Find each white blood cell.
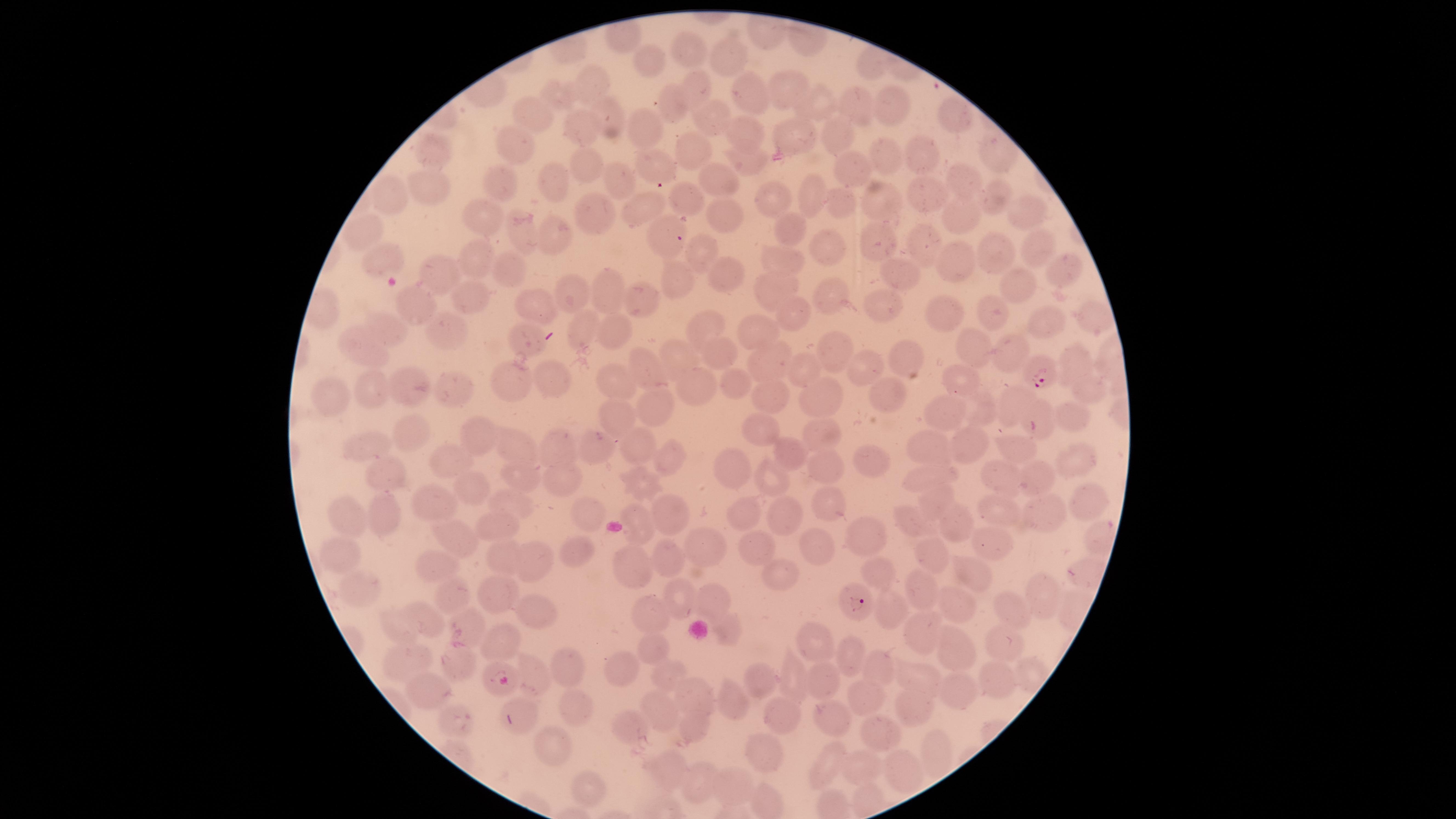

No white blood cells identified.

Approximate marker points as (x, y) in pixels. Parasitized red blood cells: (654, 169), (670, 237), (1041, 369), (854, 596). Uninfected red blood cells: (692, 49), (728, 56), (649, 60), (599, 82), (697, 87), (789, 87), (748, 93), (561, 94), (820, 102), (888, 102), (672, 105), (857, 105), (530, 113), (609, 118), (958, 118), (711, 120), (643, 123), (748, 130), (582, 131), (793, 133), (839, 133), (514, 140), (434, 149), (693, 151), (993, 154), (888, 155), (750, 157), (923, 158), (845, 163), (587, 166), (554, 177), (618, 177), (710, 178), (963, 178), (500, 183), (427, 185), (921, 193), (388, 194), (995, 194), (811, 196), (878, 196), (687, 199), (844, 201), (772, 202), (638, 210), (1017, 212), (726, 213), (595, 214), (487, 221), (965, 221), (792, 230), (551, 233), (367, 234), (520, 234), (1038, 240), (879, 241), (924, 241), (827, 247), (996, 248), (696, 250), (381, 257), (957, 258), (471, 260), (781, 260), (1068, 268), (508, 270), (899, 272), (436, 273), (728, 275), (1013, 277), (682, 283), (604, 289), (773, 290), (571, 292), (472, 298), (831, 299), (643, 301), (416, 304), (878, 305), (536, 306), (989, 310), (793, 312), (943, 313), (1098, 316), (1043, 320), (384, 325), (584, 325), (704, 328), (445, 329), (611, 331), (758, 332), (528, 336), (973, 340), (359, 341), (828, 347), (1001, 348), (718, 353), (912, 354), (1072, 354), (678, 356), (768, 363), (645, 365), (865, 366), (803, 368), (555, 381), (616, 381), (960, 382), (735, 383), (515, 384), (374, 386), (450, 387), (404, 388), (698, 388), (890, 392), (1089, 393), (325, 395), (771, 395), (828, 395), (1019, 400), (653, 405), (984, 408), (943, 413), (1040, 415), (614, 416), (1077, 421), (762, 428), (821, 429), (410, 431), (478, 436), (962, 442), (641, 443), (364, 445), (557, 445), (595, 446), (929, 446), (1016, 446), (517, 449), (671, 451), (786, 452), (450, 457), (1073, 462), (866, 463), (737, 466), (830, 467), (998, 474), (1037, 474), (385, 475), (926, 476), (517, 477), (777, 478), (564, 480), (465, 482), (640, 482), (1084, 495), (428, 501), (830, 501), (929, 503), (513, 506), (746, 509), (381, 512), (593, 512), (668, 513), (785, 513), (1004, 513), (349, 515), (1046, 516), (954, 518), (910, 521), (490, 524), (638, 526), (1100, 537), (458, 538), (866, 538), (987, 542), (821, 544), (706, 545), (757, 545), (571, 549), (338, 553), (499, 553), (929, 556), (533, 557), (436, 562), (668, 562), (631, 569), (969, 570), (880, 573), (781, 574), (358, 588), (921, 589), (487, 593), (1045, 593), (708, 597), (682, 598), (460, 603), (959, 603), (887, 607), (535, 612), (1008, 612), (652, 614), (424, 619), (472, 624), (396, 625), (724, 627), (922, 631), (813, 638), (494, 643), (1006, 645), (653, 649), (847, 649), (951, 649), (876, 660), (411, 661), (455, 662), (561, 667), (623, 669), (534, 672), (664, 673), (794, 675), (917, 676), (996, 678), (755, 680), (827, 680), (491, 684), (952, 689), (427, 691), (695, 693), (861, 696), (732, 699), (576, 706), (914, 708), (519, 709), (658, 711), (781, 714), (830, 718), (449, 721), (692, 727), (633, 728), (877, 731), (563, 745), (935, 752), (762, 753), (828, 762), (858, 767), (668, 768), (904, 771), (697, 779), (587, 787), (731, 789), (867, 799). Circular visible region. Image is 1456×819 pixels. Thin smear of blood. Species: Plasmodium falciparum. Giemsa-stained preparation. One field of view of the specimen. Photographed with a smartphone camera through the microscope eyepiece. Presence: malaria parasites identified.